Name the parasite shown.
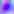

This is Toxoplasma gondii.

modality = micrograph
magnification = 400x